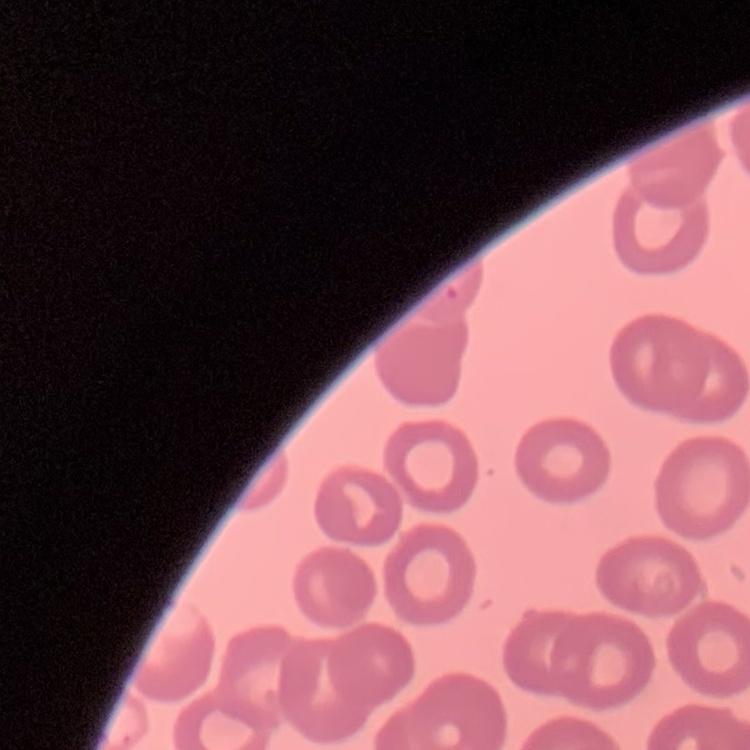
The red blood cells exhibit no rouleaux formation. Field's or Giemsa stain. One tile cut from a larger photomicrograph. Thin peripheral smear.